Assess the morphology of the red blood cells.
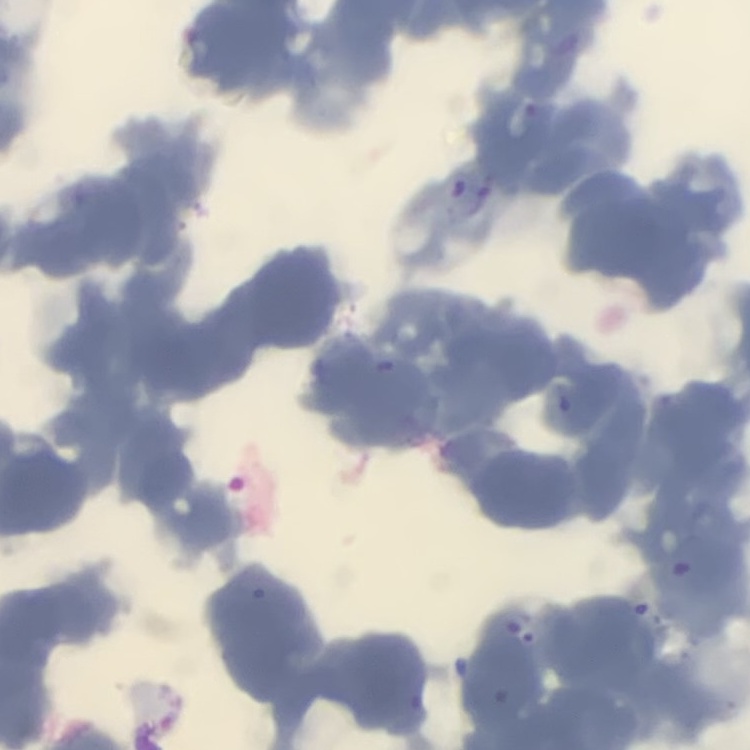
They show rouleaux formation.

preparation: thin peripheral smear
stain: Field's or Giemsa
image_type: square crop of a larger photomicrograph